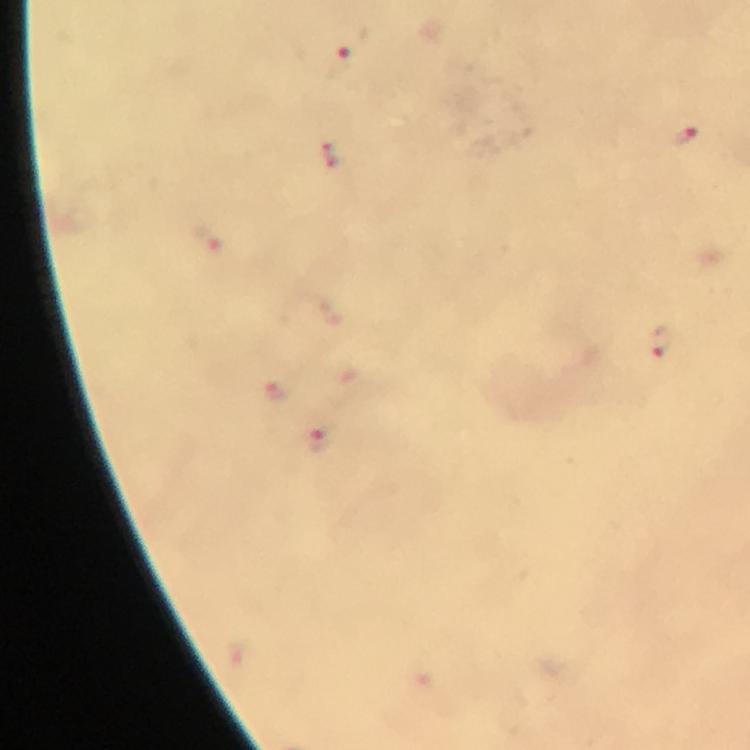

Approximate centers as (x, y) in pixels.
Summary:
  - Plasmodium parasite locations: (352, 43), (685, 136), (331, 154), (206, 237), (659, 341), (275, 392), (321, 439)
  - Capture: smartphone photograph through a microscope
  - Context: from a malaria diagnostic workup
  - Preparation: thick blood film
  - Cropped from: one field of view
  - Immersion oil: applied
  - Magnification: 100x
  - Image size: 750×750 pixels
  - Stain: Giemsa